Name the parasite shown.
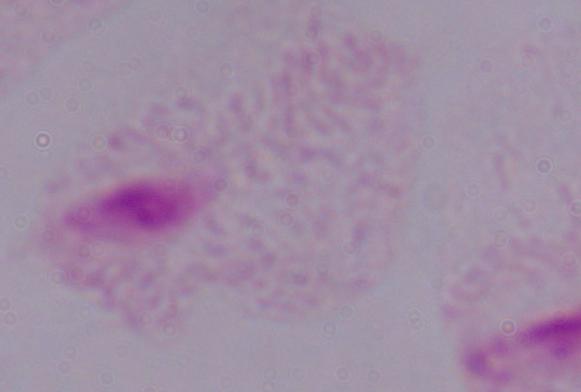

A trichomonad.

Summary:
  - Magnification: 1000x
  - Modality: micrograph